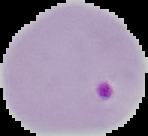
Cell region segmented out of the field of view; the surrounding area is masked to black. Image is 148×136 pixels. From a thin blood smear. Malaria status: parasitized.